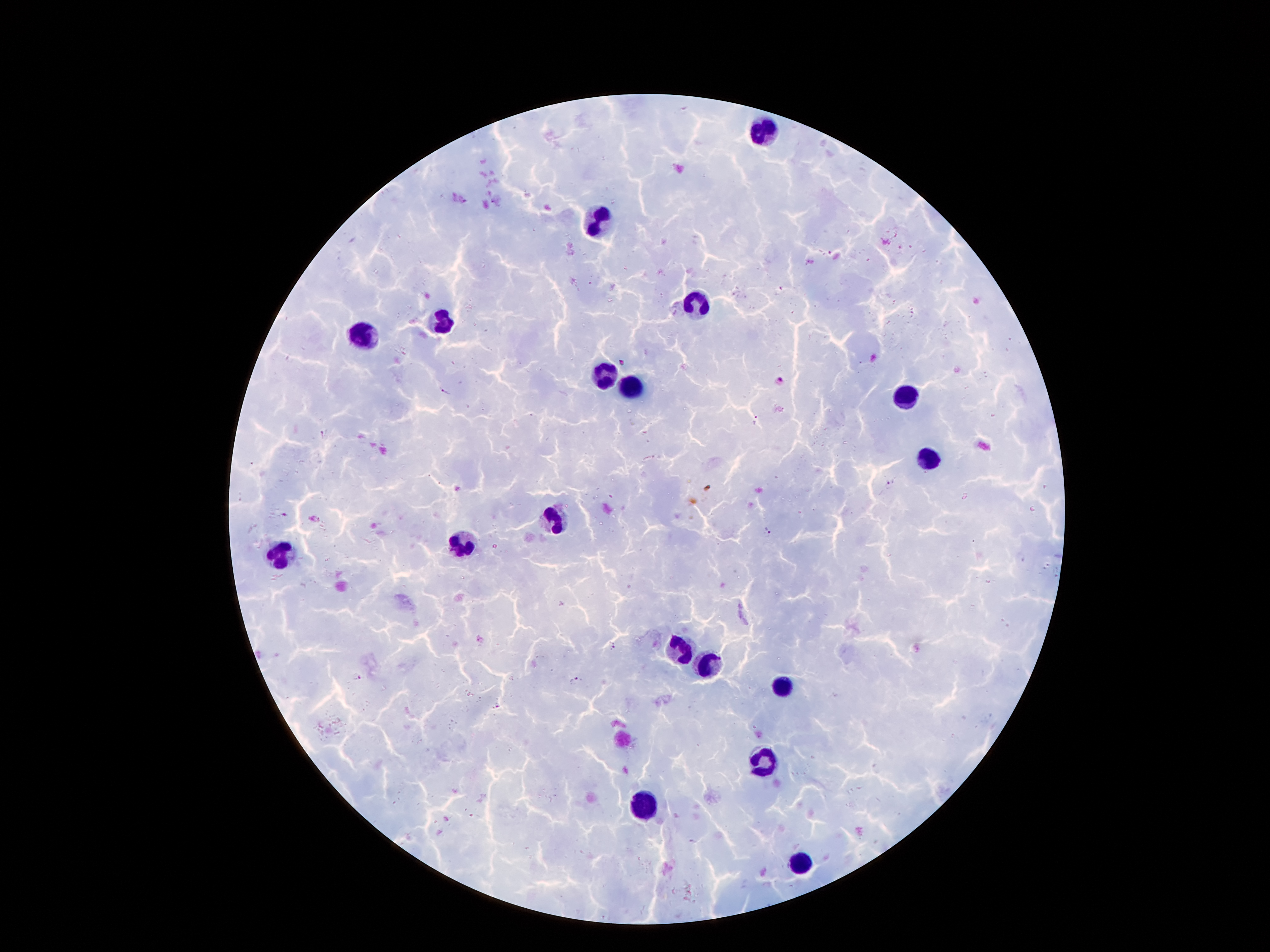

Approximate object centers, in pixels from the top-left corner. Plasmodium parasite locations: (x=781, y=379), (x=444, y=393), (x=755, y=420), (x=321, y=434), (x=891, y=482), (x=769, y=532), (x=611, y=645), (x=357, y=677), (x=576, y=680), (x=499, y=706). Leukocyte locations: (x=767, y=128), (x=599, y=222), (x=696, y=302), (x=449, y=322), (x=364, y=334), (x=602, y=373), (x=634, y=385), (x=902, y=399), (x=925, y=459), (x=556, y=516), (x=459, y=543), (x=279, y=556), (x=680, y=650), (x=709, y=666), (x=783, y=686), (x=764, y=762), (x=645, y=808), (x=798, y=865). Giemsa-stained preparation. Image is 1270×952 pixels. 100x magnification. Smartphone photograph taken through the microscope eyepiece. Thick blood film. Patient malaria status: positive for Plasmodium falciparum. One field from this slide.